Assess this cell for malaria.
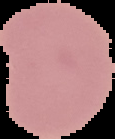
It is uninfected.

From a thin blood smear. Image is 115×139 pixels. The area outside the segmented cell region is set to black.